Point out each Plasmodium parasite.
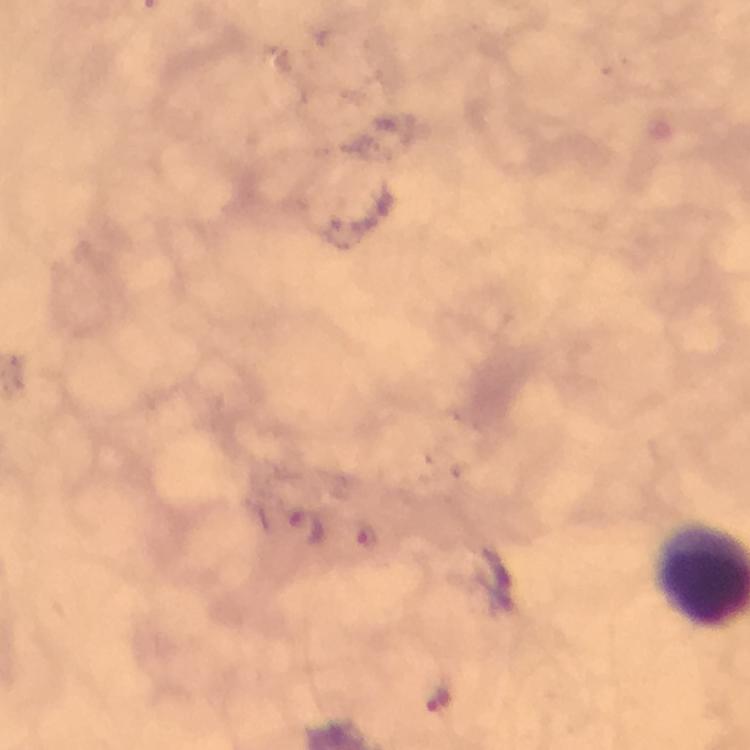
Approximate centers as (x, y) in pixels.
Plasmodium parasites: (306, 527), (366, 538), (437, 697).

Summary:
  - Stain: Giemsa
  - Preparation: thick smear
  - Context: from a malaria diagnostic workup
  - Capture: smartphone camera through the microscope
  - Magnification: 100x
  - Immersion oil: used
  - Image size: 750×750 pixels
  - Cropped from: a single field of view